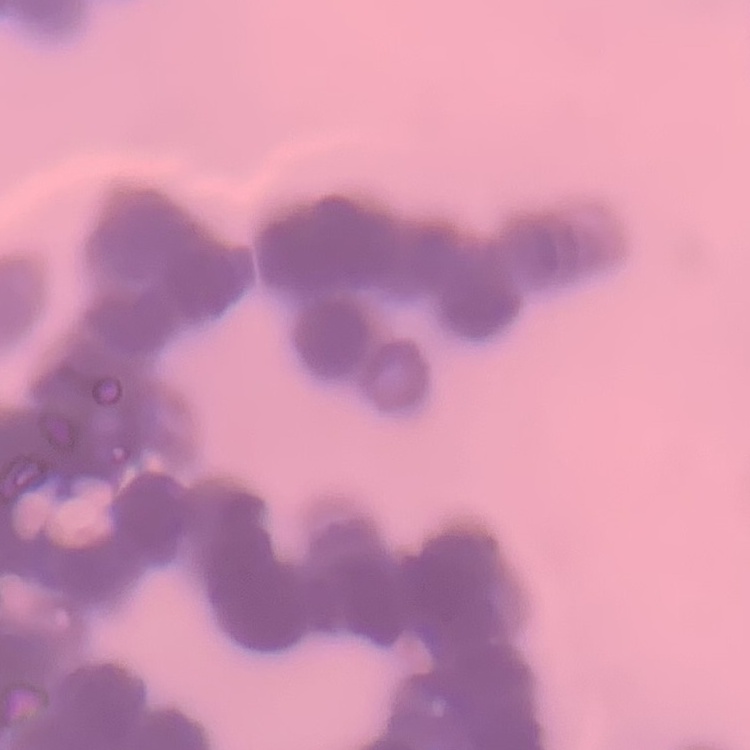 The red blood cells show rouleaux formation. Field's or Giemsa stain. Thin blood film. Square crop of a larger photomicrograph.